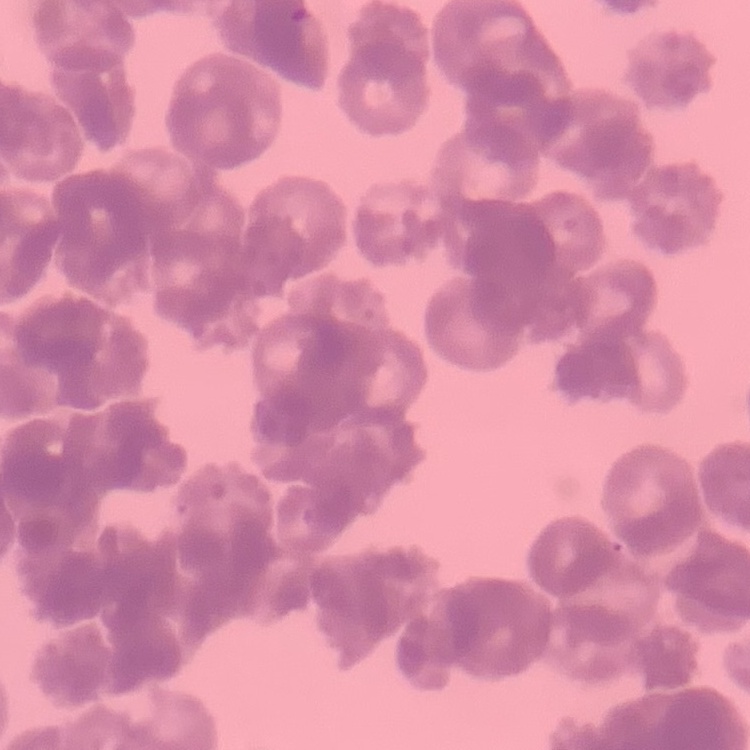

Summary:
  - Erythrocyte morphology: rouleaux formation
  - Image type: one tile cut from a larger photomicrograph
  - Preparation: thin blood film
  - Stain: Field's or Giemsa